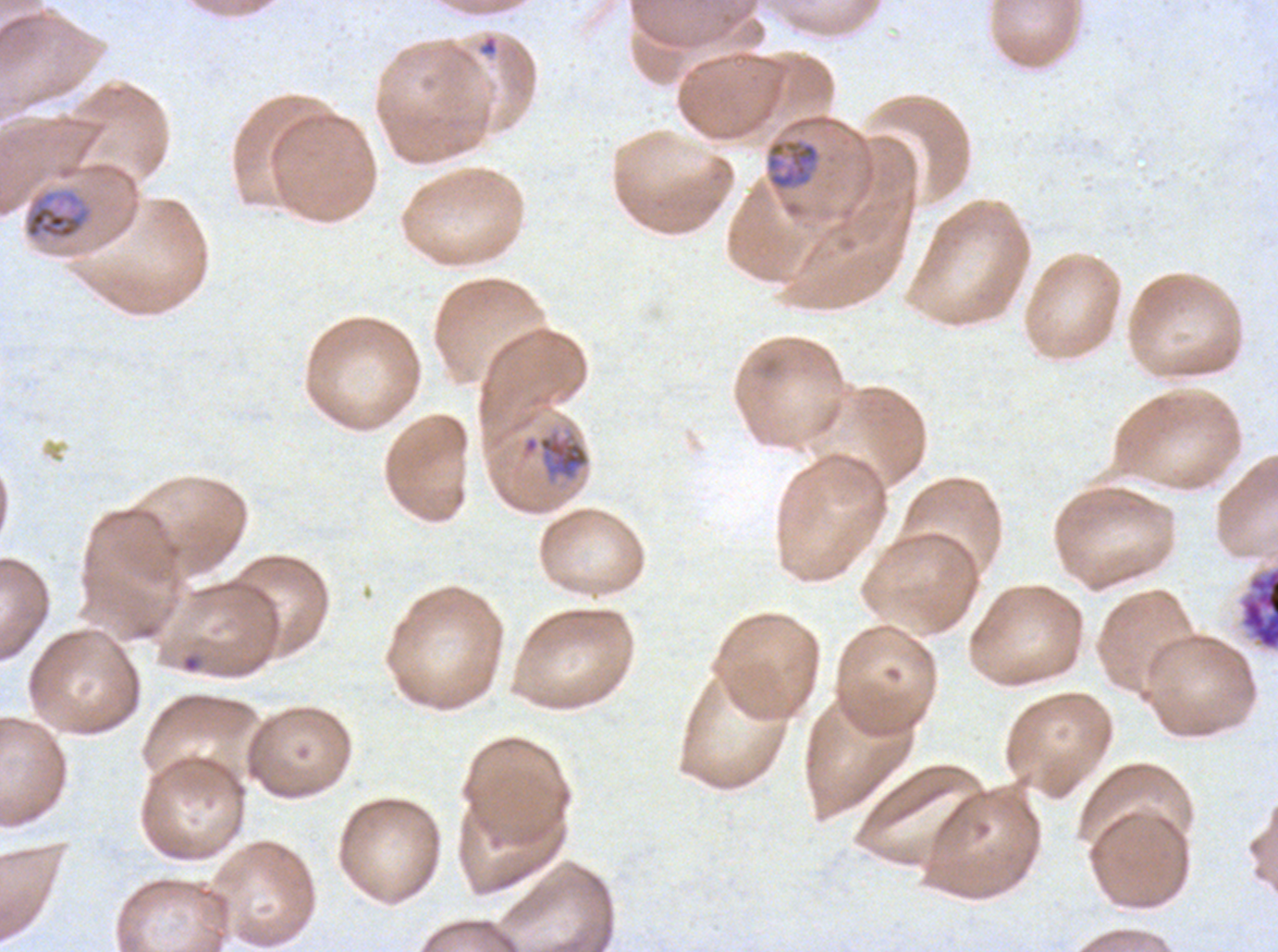

Approximate bounding rectangles given as corner coordinates in pixels from the top-left. Mid trophozoite locations: (x1=765, y1=139, x2=820, y2=190), (x1=23, y1=189, x2=93, y2=241), (x1=522, y1=430, x2=590, y2=482). Ring locations: (x1=182, y1=654, x2=201, y2=673). Segmenter locations: (x1=1237, y1=565, x2=1277, y2=653). Image is 1278×952 pixels. Thin blood smear. One sub-image of a larger composite. Giemsa-stained preparation. Life-cycle stages observed: ring, mid trophozoite, segmenter. Ex-vivo P. falciparum culture from a patient in The Gambia, grown for 24 to 48 hours.